Locate and identify every blood parasite.
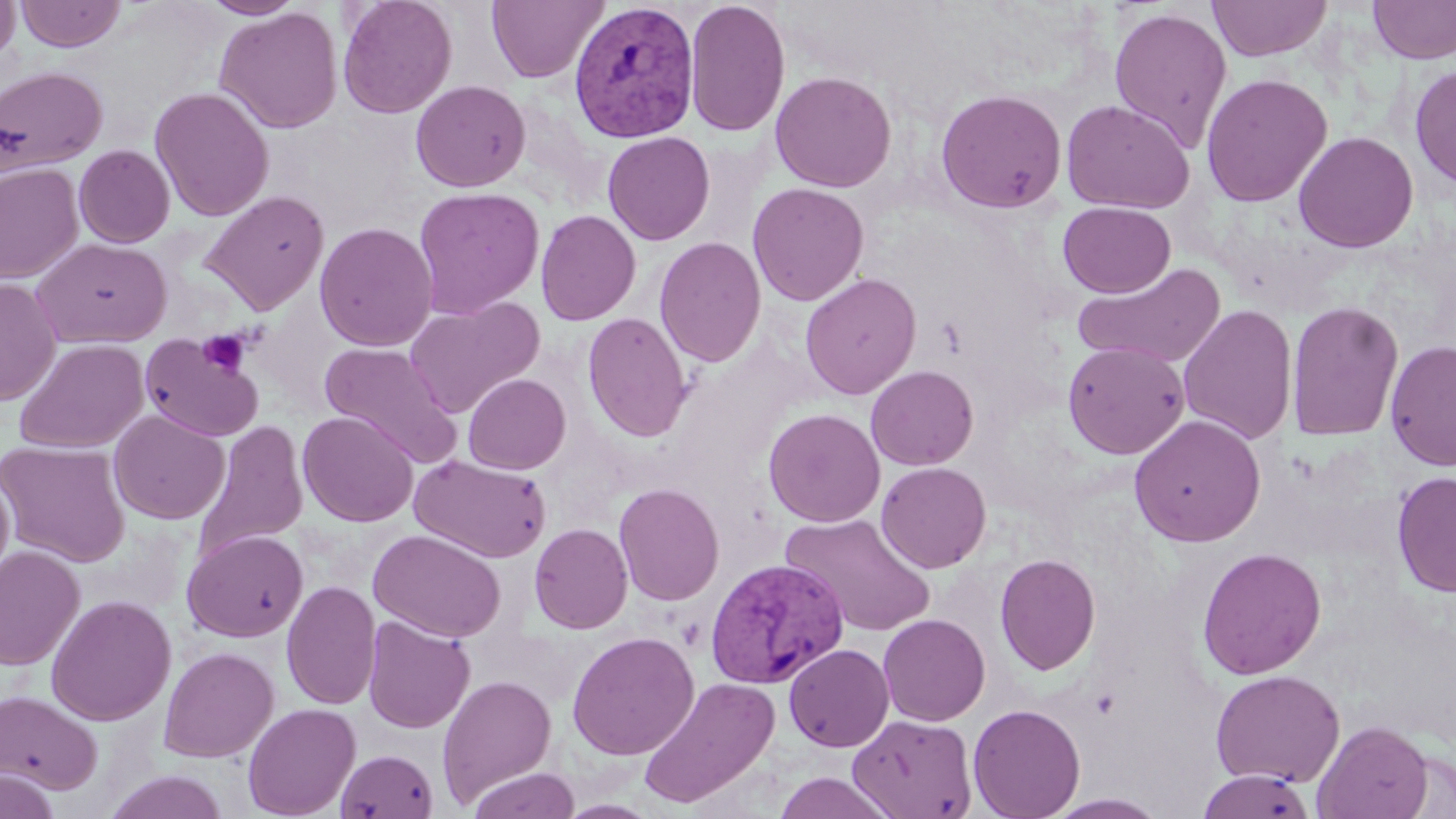

Approximate bounding boxes as [x1, y1, x2, y2] in pixels.
Plasmodium vivax-infected red blood cells: [568, 1, 700, 143], [705, 557, 849, 689].
No Plasmodium falciparum, Plasmodium ovale, Plasmodium malariae, Babesia divergens, or Trypanosoma brucei observed.

{
  "slide_level_diagnosis": "Plasmodium vivax",
  "modality": "optical microscopy",
  "magnification": "1000x",
  "field_of_view": "single",
  "platelet_locations": "approximate bounding boxes as [x1, y1, x2, y2] in pixels: [197, 329, 253, 376]",
  "uninfected_red_blood_cell_locations": "approximate bounding boxes as [x1, y1, x2, y2] in pixels: [0, 0, 20, 68], [15, 0, 126, 52], [201, 0, 304, 19], [337, 0, 457, 118], [486, 0, 608, 84], [685, 0, 791, 138], [1207, 0, 1333, 61], [1367, 0, 1456, 63], [213, 6, 343, 134], [1108, 7, 1232, 152], [1409, 62, 1456, 192], [0, 66, 108, 175], [770, 71, 897, 192], [1200, 72, 1333, 208], [410, 80, 531, 192], [150, 86, 274, 222], [934, 88, 1068, 214], [1061, 100, 1196, 213], [1293, 131, 1419, 252], [602, 132, 715, 245], [74, 144, 175, 248], [0, 162, 83, 284], [747, 182, 869, 306], [412, 186, 545, 319], [198, 190, 329, 316], [1058, 201, 1176, 298], [535, 209, 641, 326], [315, 222, 438, 351], [654, 236, 766, 368], [33, 238, 172, 348], [1071, 263, 1227, 368], [800, 272, 922, 400], [0, 277, 61, 406], [405, 297, 544, 417], [1286, 299, 1404, 442], [1177, 302, 1298, 445], [582, 312, 692, 442], [140, 332, 265, 442], [14, 338, 148, 454], [1385, 340, 1456, 471], [1062, 341, 1189, 459], [319, 342, 461, 466], [866, 365, 978, 470], [463, 373, 571, 474], [763, 408, 885, 527], [108, 410, 229, 525], [298, 411, 417, 526], [1129, 414, 1266, 547], [192, 420, 309, 561], [0, 440, 131, 567], [410, 454, 552, 563], [876, 462, 992, 573], [0, 466, 15, 590], [1391, 470, 1456, 598], [613, 482, 724, 606], [780, 512, 936, 637], [529, 524, 633, 634], [368, 528, 506, 643], [182, 530, 308, 642], [0, 545, 85, 671], [1196, 546, 1327, 679], [995, 553, 1101, 675], [281, 580, 381, 710], [45, 594, 176, 726], [877, 613, 991, 726], [363, 616, 475, 734], [566, 630, 700, 760], [784, 643, 894, 752], [159, 646, 279, 762], [1210, 669, 1345, 788], [437, 673, 557, 807], [638, 676, 780, 808], [0, 688, 103, 794], [242, 703, 360, 818], [968, 703, 1086, 819], [847, 714, 978, 819], [1312, 718, 1433, 818], [335, 748, 439, 819], [0, 767, 61, 819], [467, 767, 581, 819], [1197, 769, 1316, 819], [103, 770, 230, 819], [772, 772, 897, 819], [1042, 792, 1170, 818], [553, 799, 665, 819]",
  "stain": "May-Grünwald-Giemsa",
  "preparation": "thin blood film",
  "image_size": "1456×819 pixels"
}